Outline each blood parasite and name the species.
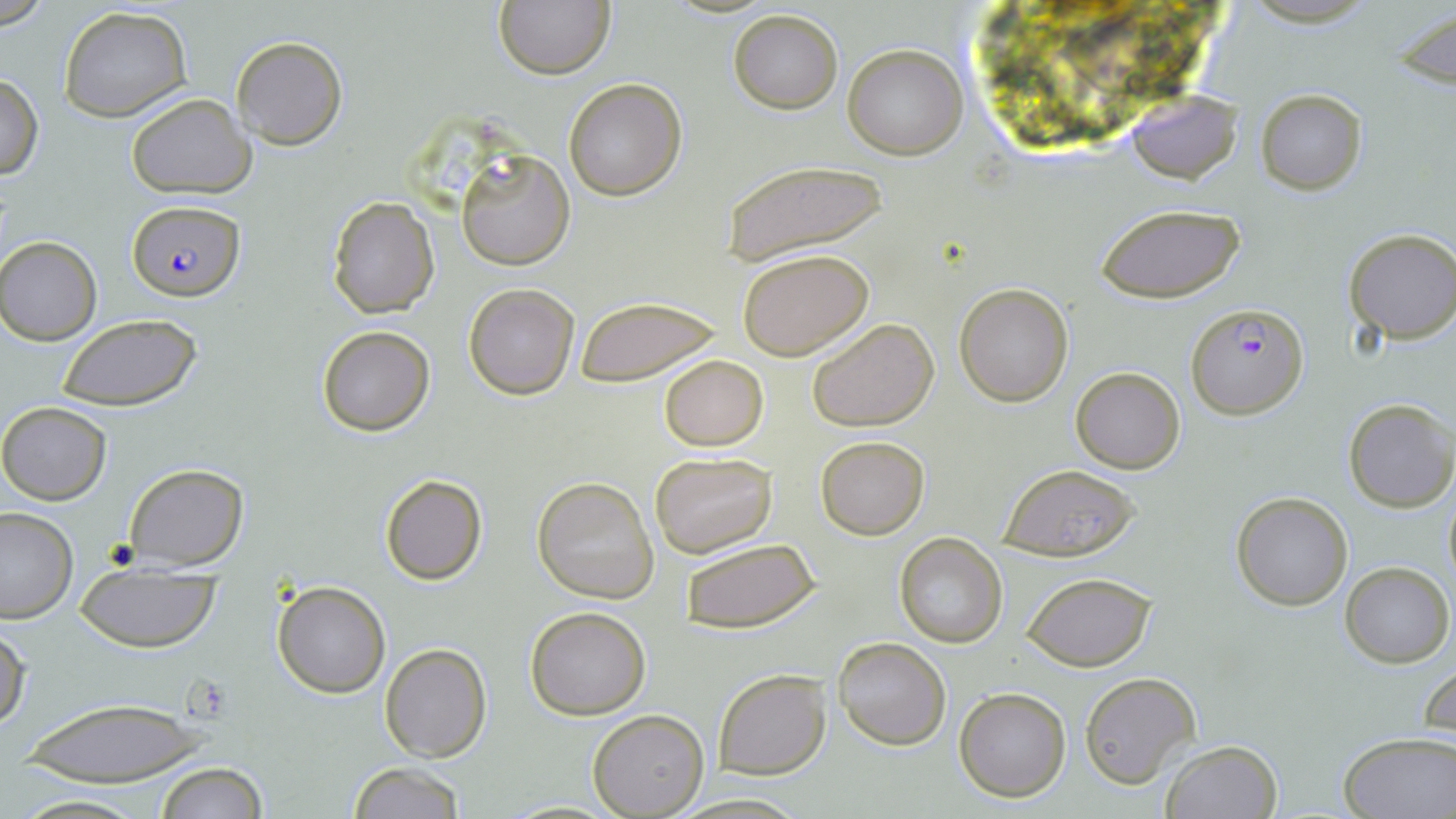
Approximate bounding boxes as (x1,y1)-(x2,y2) corner pairs in pixels.
Plasmodium falciparum-infected red blood cells: (128,197)-(244,303), (1187,304)-(1308,420).
No Plasmodium ovale, Plasmodium malariae, Plasmodium vivax, Babesia divergens, or Trypanosoma brucei observed.

Summary:
  - Uninfected red blood cell locations: (2,0)-(50,29), (493,1)-(615,80), (59,5)-(192,123), (1390,5)-(1456,90), (728,9)-(843,115), (230,35)-(348,152), (842,44)-(966,161), (0,74)-(44,181), (563,78)-(687,202), (1256,89)-(1367,195), (1128,92)-(1241,183), (125,94)-(255,199), (456,147)-(576,271), (718,158)-(890,267), (326,196)-(441,319), (1095,203)-(1247,305), (1344,228)-(1456,345), (1,236)-(101,344), (738,248)-(874,361), (954,281)-(1074,407), (463,283)-(579,401), (573,293)-(724,386), (54,313)-(203,410), (805,317)-(941,432), (315,323)-(436,438), (659,355)-(768,451), (1070,366)-(1186,474), (1342,398)-(1455,513), (0,402)-(111,505), (816,435)-(929,539), (650,451)-(777,557), (123,463)-(248,570), (998,463)-(1142,562), (379,473)-(487,586), (532,475)-(660,604), (1442,485)-(1456,594), (1230,491)-(1356,610), (0,507)-(77,623), (894,532)-(1008,649), (681,539)-(820,633), (1339,562)-(1452,667), (76,567)-(221,654), (1021,572)-(1157,673), (272,580)-(390,698), (524,606)-(652,719), (0,623)-(29,734), (831,637)-(952,751), (379,642)-(493,763), (1420,659)-(1456,756), (713,669)-(831,780), (1080,671)-(1199,787), (953,686)-(1072,802), (9,695)-(220,784), (588,709)-(709,817), (1340,732)-(1455,818), (1161,740)-(1283,819), (156,762)-(269,818), (347,762)-(469,819), (4,793)-(157,819)
  - Slide-level diagnosis: Plasmodium falciparum
  - Magnification: 1000x
  - Stain: May-Grünwald-Giemsa
  - Preparation: thin blood smear
  - Modality: optical microscopy
  - Image size: 1456×819 pixels
  - Field of view: one of a larger specimen